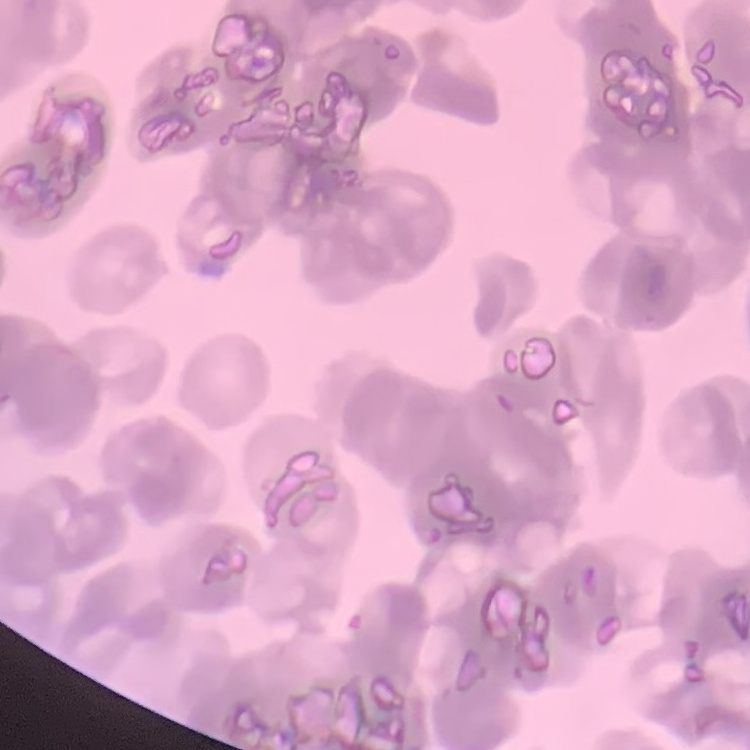

Summary:
  - Erythrocyte morphology: rouleaux formation
  - Preparation: thin blood film
  - Stain: Field's or Giemsa
  - Image type: one tile cut from a larger photomicrograph